Locate every Plasmodium falciparum-infected red blood cell.
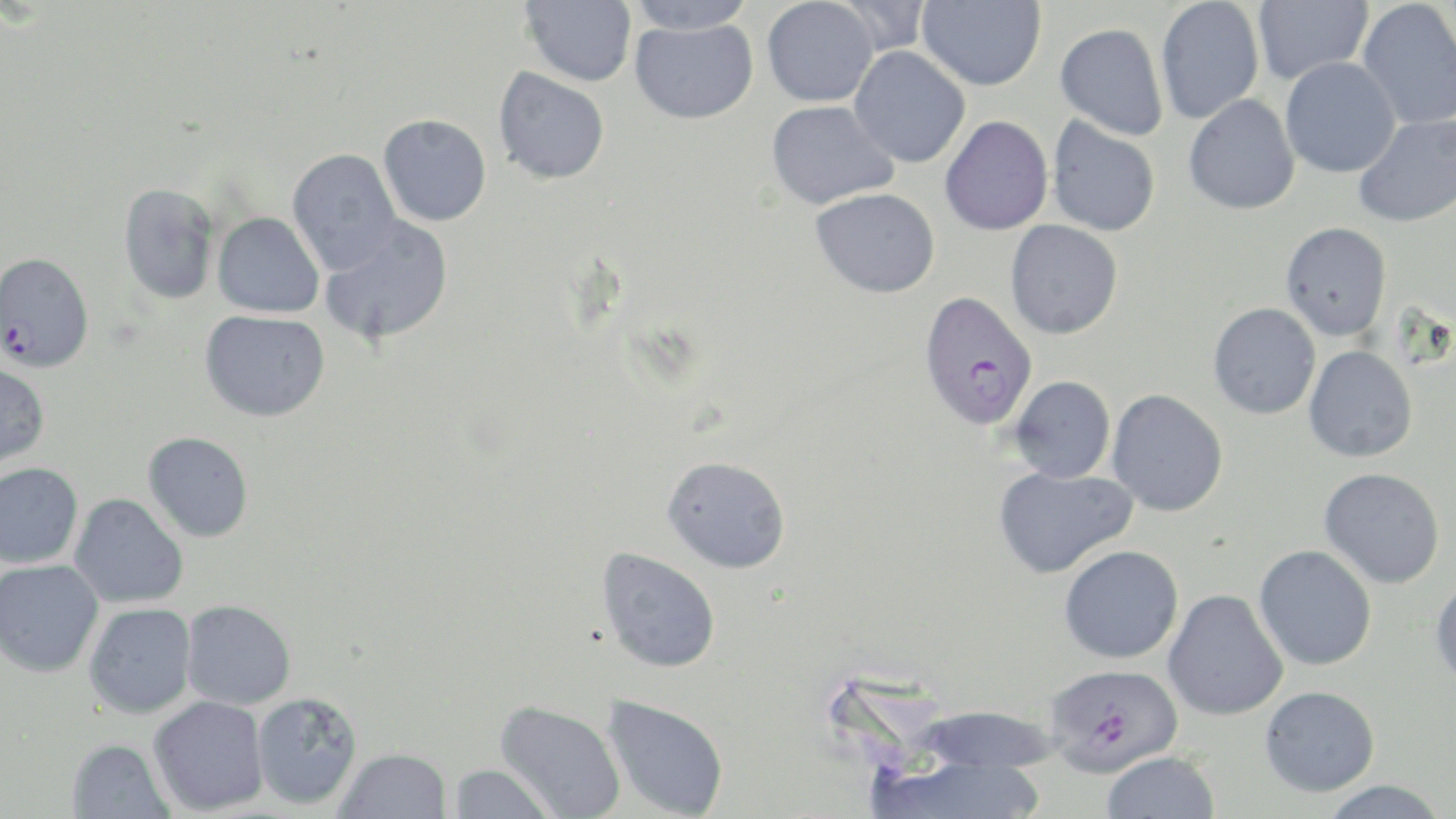

Approximate bounding boxes as (x1,y1)-(x2,y2) corner pairs in pixels.
Plasmodium falciparum-infected red blood cells: (0,252)-(95,373), (918,290)-(1039,431), (1044,663)-(1183,775).

Uninfected red blood cell locations: (626,0)-(755,34), (762,0)-(879,107), (830,0)-(933,56), (917,0)-(1046,91), (1155,0)-(1264,125), (1251,0)-(1373,86), (520,1)-(638,87), (1356,1)-(1456,131), (629,18)-(758,124), (1055,23)-(1169,141), (849,46)-(971,168), (1280,58)-(1400,178), (493,67)-(610,185), (1183,95)-(1301,215), (766,100)-(899,209), (1353,113)-(1456,228), (378,114)-(492,227), (939,115)-(1053,236), (1047,116)-(1161,236), (287,148)-(403,275), (117,182)-(220,305), (810,188)-(940,298), (213,212)-(324,318), (319,216)-(454,346), (1005,219)-(1123,339), (1280,221)-(1392,341), (1208,302)-(1321,419), (200,310)-(330,421), (1303,345)-(1418,463), (0,363)-(50,467), (1009,375)-(1115,483), (1107,389)-(1229,517), (143,431)-(254,542), (662,455)-(791,573), (0,462)-(83,569), (993,464)-(1137,579), (1318,467)-(1446,589), (69,493)-(189,608), (1059,544)-(1184,664), (1254,544)-(1377,670), (596,547)-(721,673), (0,559)-(104,677), (1430,575)-(1456,687), (1162,588)-(1289,721), (180,599)-(296,709), (84,602)-(197,718), (1259,685)-(1380,796), (251,691)-(363,809), (602,694)-(730,819), (147,695)-(269,816), (495,700)-(626,818), (919,705)-(1061,773), (65,738)-(176,819), (334,747)-(452,819), (1101,750)-(1221,818), (870,755)-(1047,819), (447,764)-(557,818), (1317,780)-(1449,819). Slide-level diagnosis: Plasmodium falciparum. Captured at 1000x magnification. May-Grünwald-Giemsa-stained preparation. Single field of view. Thin blood film. Optical microscopy. Image is 1456×819 pixels.